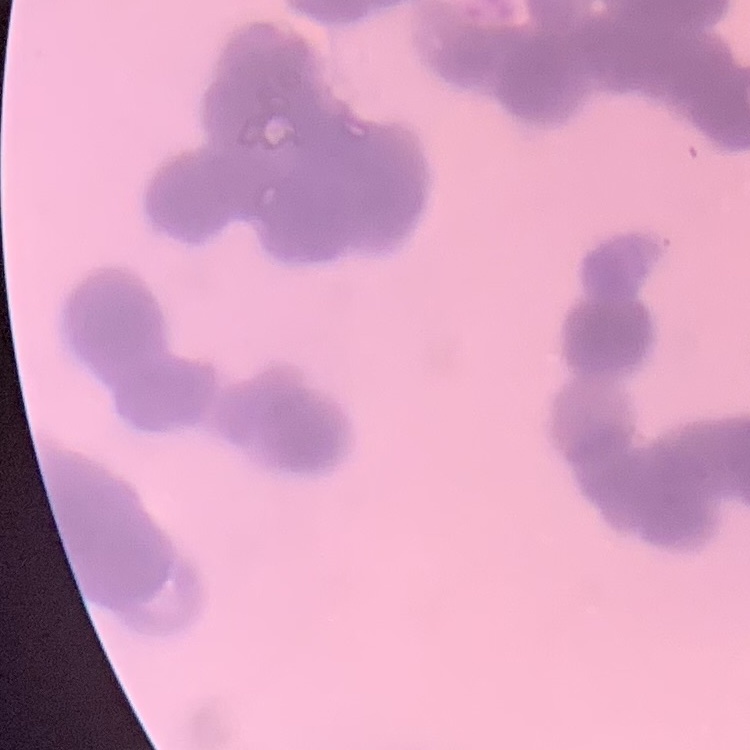
{
  "red_blood_cell_morphology": "rouleaux formation",
  "preparation": "thin blood smear",
  "image_type": "one tile cut from a larger photomicrograph",
  "stain": "Field's or Giemsa"
}